Classify this cell by malaria status.
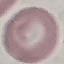

Uninfected.

Summary:
  - Image type: automatically extracted cell patch, resized to 64 × 64 pixels
  - Capture: smartphone camera at the microscope eyepiece
  - Stain: Giemsa
  - Preparation: thin blood film